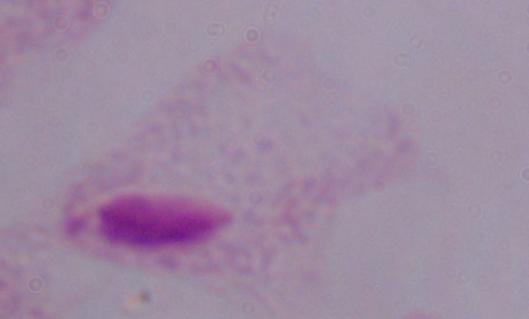
Summary:
  - Modality: photomicrograph
  - Magnification: 1000x
  - Identification: trichomonad